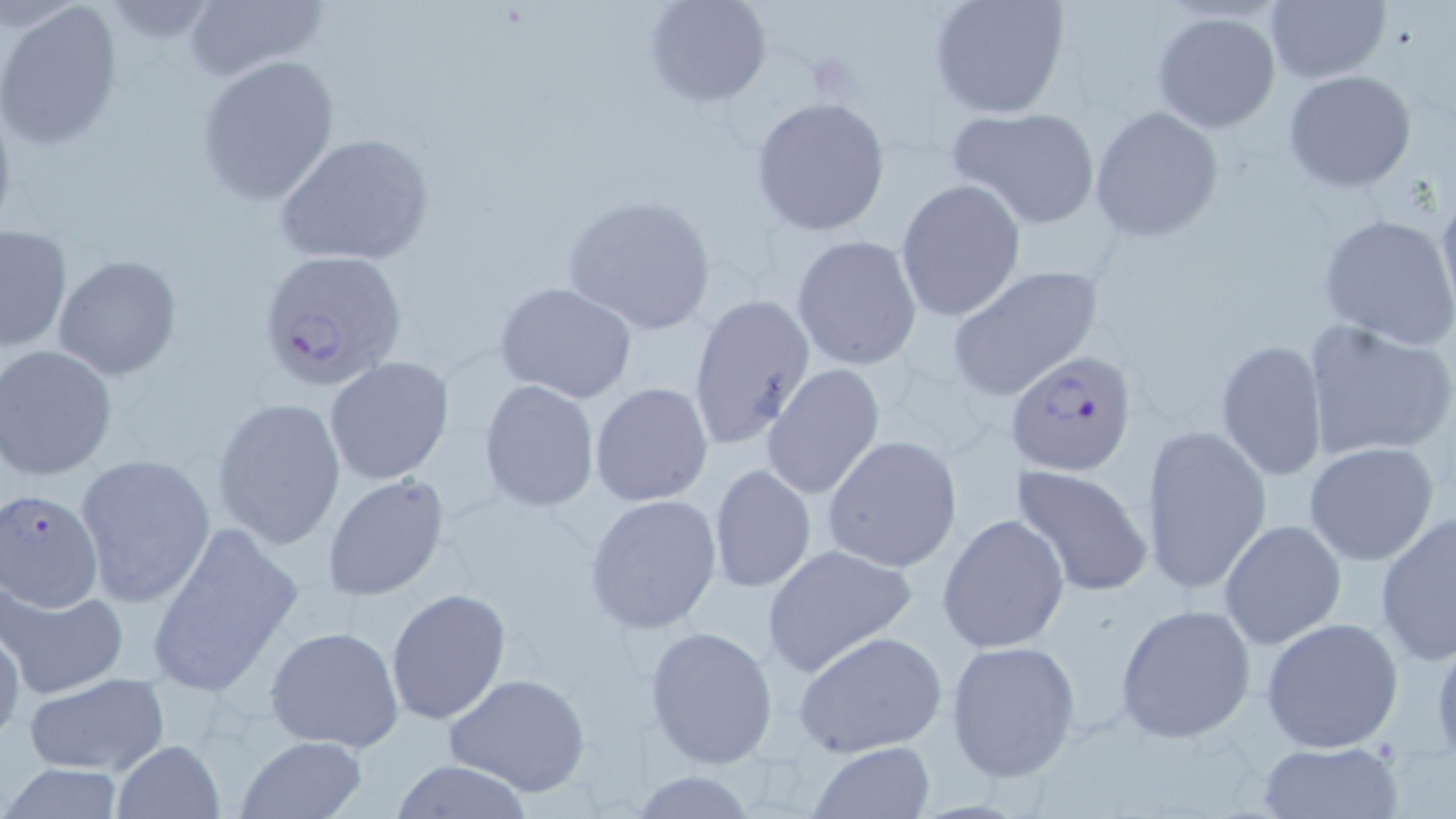
Summary:
  - Coordinate format: approximate bounding boxes as (x1, y1, x2, y2) in pixels
  - Uninfected red blood cell locations: (645, 0, 772, 109), (928, 0, 1071, 118), (180, 1, 328, 81), (1, 2, 124, 151), (1264, 2, 1390, 85), (1151, 9, 1283, 134), (195, 55, 341, 206), (1282, 69, 1419, 192), (749, 95, 891, 236), (946, 104, 1102, 230), (1089, 106, 1225, 244), (273, 133, 434, 267), (894, 179, 1025, 324), (1436, 187, 1456, 321), (560, 195, 719, 337), (1318, 214, 1456, 351), (1, 225, 72, 353), (791, 234, 922, 370), (52, 255, 183, 378), (945, 265, 1103, 401), (494, 280, 639, 404), (687, 293, 815, 451), (1303, 318, 1456, 465), (1214, 340, 1326, 481), (0, 344, 118, 480), (325, 356, 455, 485), (762, 365, 886, 501), (479, 379, 601, 512), (589, 382, 713, 507), (213, 396, 348, 551), (1140, 424, 1272, 595), (823, 435, 962, 573), (1303, 442, 1441, 567), (74, 451, 216, 608), (1011, 463, 1154, 598), (707, 464, 818, 595), (322, 472, 451, 601), (584, 494, 723, 634), (1375, 509, 1456, 665), (938, 512, 1072, 653), (144, 519, 304, 698), (1218, 519, 1346, 649), (761, 543, 919, 677), (2, 581, 127, 700), (386, 587, 511, 725), (1114, 603, 1258, 744), (1261, 617, 1404, 753), (0, 618, 25, 747), (264, 625, 405, 752), (644, 627, 779, 768), (793, 629, 947, 759), (1429, 630, 1456, 767), (944, 638, 1080, 782), (445, 671, 593, 796), (20, 673, 172, 778), (235, 734, 369, 818), (111, 738, 224, 819), (1257, 738, 1406, 817), (805, 740, 938, 818), (386, 760, 539, 818), (0, 764, 130, 818)
  - Plasmodium falciparum-infected red blood cell locations: (255, 248, 408, 391), (1007, 351, 1138, 476), (1, 487, 106, 612)
  - Platelet locations: (805, 55, 856, 100)
  - Slide-level diagnosis: Plasmodium falciparum
  - Image size: 1456×819 pixels
  - Stain: May-Grünwald-Giemsa
  - Modality: optical microscopy
  - Field of view: single
  - Preparation: thin blood film
  - Magnification: 1000x